Locate every blood parasite and identify its species.
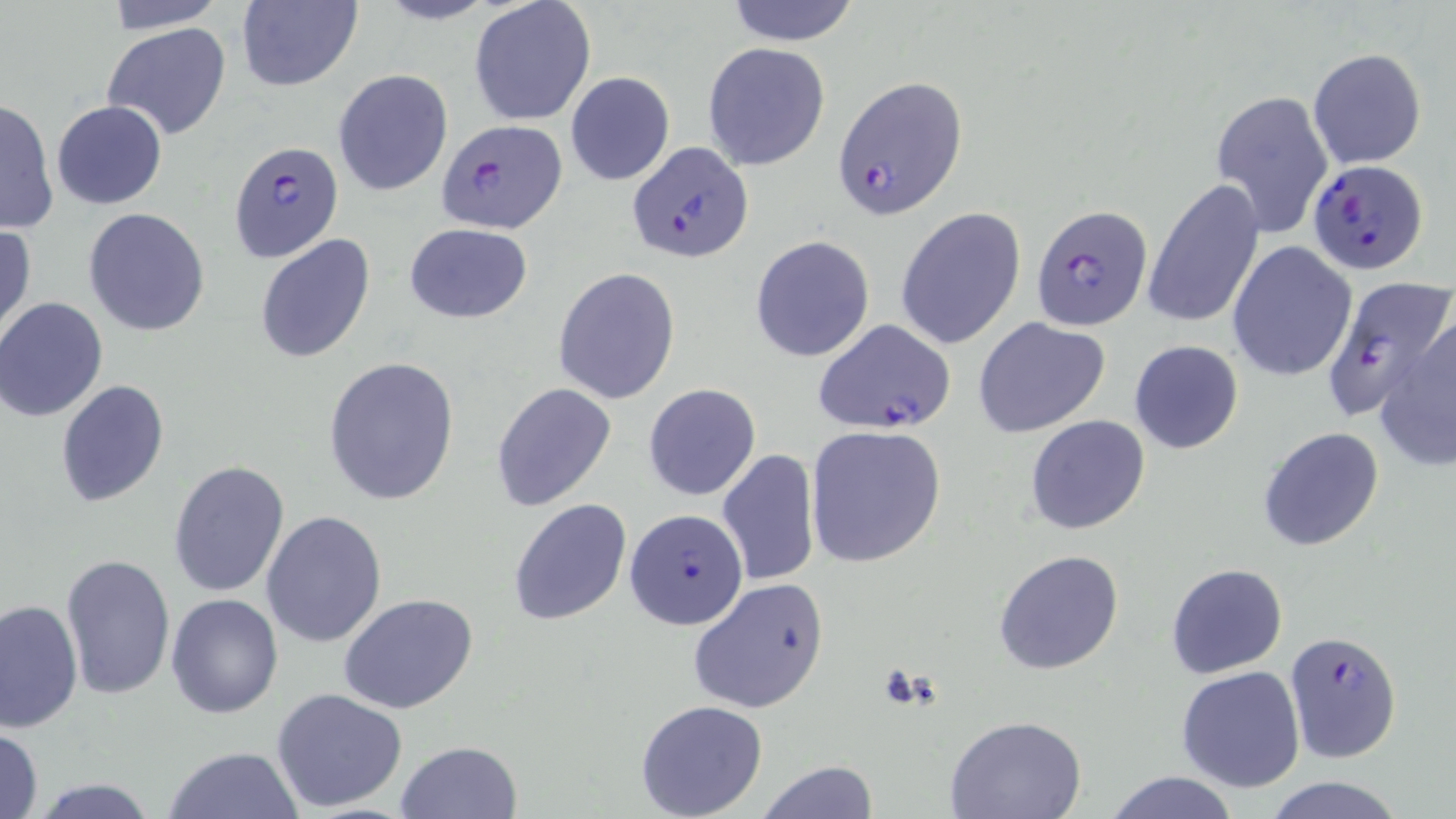
Approximate bounding boxes as named x1/y1/x2/y2 corners in pixels.
Plasmodium falciparum-infected red blood cells: (x1=834, y1=76, x2=965, y2=218), (x1=434, y1=117, x2=567, y2=233), (x1=627, y1=141, x2=755, y2=263), (x1=230, y1=143, x2=342, y2=260), (x1=1307, y1=158, x2=1429, y2=273), (x1=1030, y1=204, x2=1152, y2=328), (x1=1322, y1=277, x2=1454, y2=418), (x1=811, y1=318, x2=956, y2=435), (x1=624, y1=510, x2=750, y2=632), (x1=1284, y1=631, x2=1403, y2=763).
No Plasmodium ovale, Plasmodium malariae, Plasmodium vivax, Babesia divergens, or Trypanosoma brucei observed.

Summary:
  - Uninfected red blood cell locations: (x1=97, y1=0, x2=230, y2=32), (x1=235, y1=0, x2=362, y2=91), (x1=469, y1=0, x2=597, y2=127), (x1=723, y1=1, x2=863, y2=45), (x1=103, y1=22, x2=232, y2=141), (x1=703, y1=42, x2=832, y2=172), (x1=1308, y1=48, x2=1428, y2=170), (x1=333, y1=69, x2=453, y2=196), (x1=565, y1=72, x2=676, y2=187), (x1=1210, y1=89, x2=1335, y2=239), (x1=0, y1=96, x2=59, y2=235), (x1=51, y1=99, x2=168, y2=209), (x1=1144, y1=179, x2=1264, y2=330), (x1=83, y1=207, x2=211, y2=336), (x1=895, y1=207, x2=1026, y2=350), (x1=0, y1=223, x2=36, y2=342), (x1=403, y1=223, x2=534, y2=324), (x1=255, y1=234, x2=376, y2=363), (x1=750, y1=236, x2=874, y2=362), (x1=1228, y1=240, x2=1356, y2=380), (x1=553, y1=268, x2=680, y2=405), (x1=0, y1=297, x2=110, y2=422), (x1=1373, y1=310, x2=1456, y2=471), (x1=973, y1=316, x2=1112, y2=437), (x1=1128, y1=340, x2=1245, y2=454), (x1=322, y1=356, x2=461, y2=507), (x1=55, y1=380, x2=169, y2=508), (x1=491, y1=382, x2=617, y2=511), (x1=643, y1=384, x2=760, y2=501), (x1=1025, y1=414, x2=1150, y2=536), (x1=805, y1=424, x2=947, y2=569), (x1=1258, y1=426, x2=1384, y2=551), (x1=717, y1=450, x2=821, y2=587), (x1=168, y1=460, x2=290, y2=597), (x1=508, y1=499, x2=632, y2=626), (x1=261, y1=510, x2=386, y2=649), (x1=994, y1=550, x2=1125, y2=675), (x1=61, y1=553, x2=175, y2=698), (x1=1165, y1=563, x2=1288, y2=678), (x1=686, y1=578, x2=831, y2=714), (x1=338, y1=593, x2=479, y2=714), (x1=166, y1=594, x2=283, y2=718), (x1=0, y1=598, x2=83, y2=735), (x1=1176, y1=666, x2=1306, y2=794), (x1=270, y1=688, x2=408, y2=812), (x1=635, y1=700, x2=768, y2=818), (x1=945, y1=715, x2=1087, y2=819), (x1=1, y1=728, x2=46, y2=818), (x1=395, y1=741, x2=523, y2=819), (x1=164, y1=747, x2=304, y2=819), (x1=754, y1=760, x2=877, y2=818), (x1=1105, y1=771, x2=1242, y2=819), (x1=1260, y1=775, x2=1408, y2=819), (x1=26, y1=778, x2=164, y2=818)
  - Slide-level diagnosis: Plasmodium falciparum
  - Field of view: single
  - Stain: May-Grünwald-Giemsa
  - Modality: light microscopy
  - Preparation: thin blood film
  - Image size: 1456×819 pixels
  - Magnification: 1000x